Name the blood parasite species.
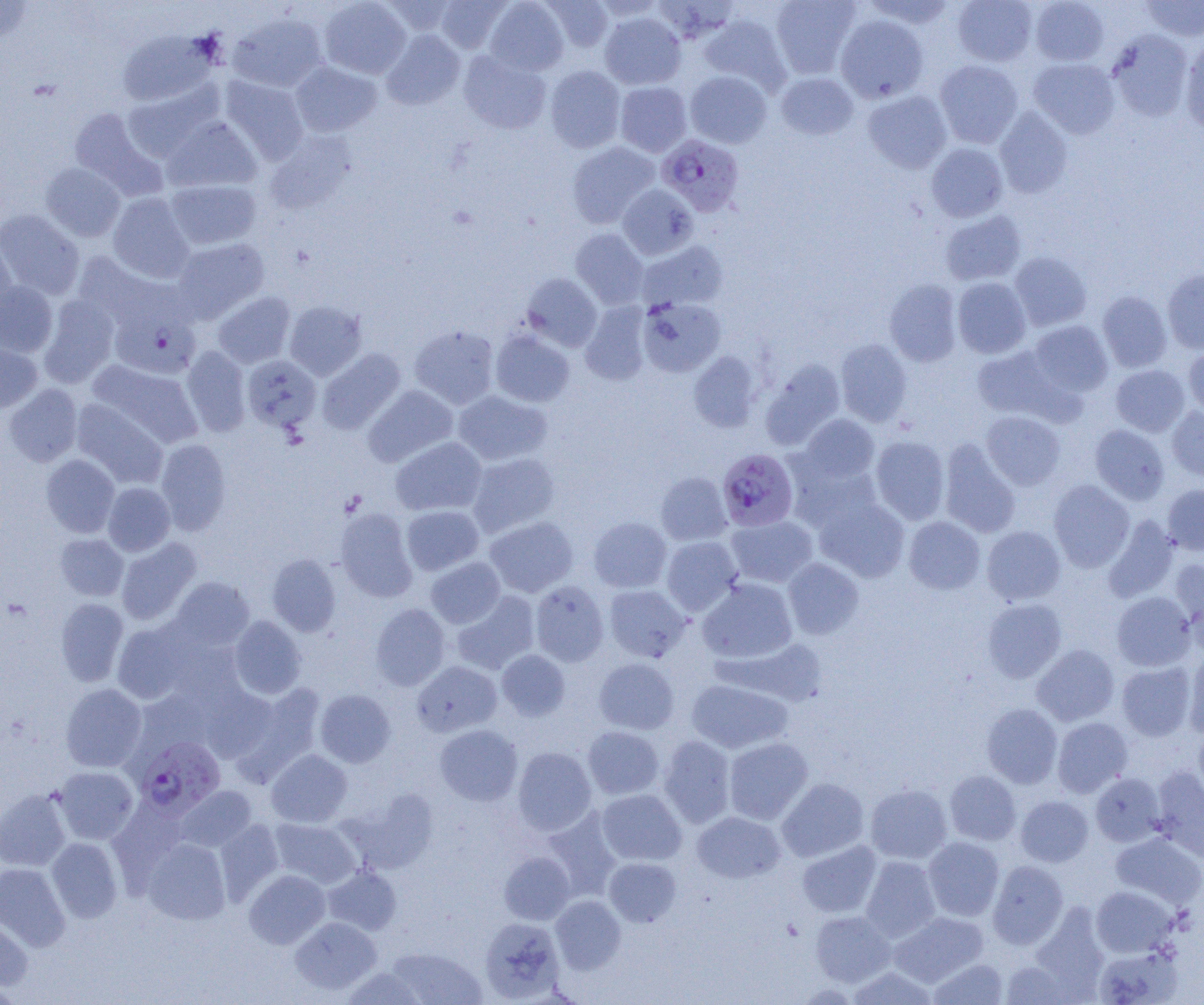

Plasmodium falciparum.

modality = light microscopy
Plasmodium falciparum-infected red blood cell locations = approximate bounding boxes as (x1,y1)-(x2,y2) corner pairs in pixels: (656,134)-(744,216), (110,304)-(201,379), (717,448)-(798,531), (134,737)-(225,817)
image size = 1204×1005 pixels
magnification = 1000x
preparation = thin blood smear
field of view = single
uninfected red blood cell locations = approximate bounding boxes as (x1,y1)-(x2,y2) corner pairs in pixels: (0,0)-(33,45), (319,0)-(411,79), (435,0)-(511,53), (484,0)-(569,76), (541,0)-(613,52), (770,0)-(860,78), (862,0)-(958,29), (952,0)-(1038,66), (1030,0)-(1109,66), (1140,0)-(1204,41), (379,1)-(460,37), (600,12)-(686,90), (229,14)-(327,92), (699,14)-(791,92), (836,14)-(929,103), (117,29)-(216,108), (381,29)-(465,110), (1107,30)-(1194,122), (1179,39)-(1204,133), (459,50)-(551,134), (1028,58)-(1120,139), (935,60)-(1023,148), (290,61)-(382,137), (545,65)-(626,152), (685,71)-(772,148), (775,72)-(859,140), (221,76)-(309,163), (615,81)-(692,156), (123,83)-(222,162), (862,89)-(952,174), (68,107)-(166,200), (993,107)-(1073,198), (162,117)-(262,193), (264,131)-(355,214), (567,141)-(660,228), (926,142)-(1008,222), (41,163)-(125,241), (165,179)-(261,249), (618,184)-(698,260), (108,193)-(194,282), (0,209)-(84,300), (940,210)-(1027,286), (570,228)-(649,309), (0,233)-(17,323), (171,238)-(270,322), (637,240)-(728,312), (72,251)-(175,336), (1009,251)-(1092,331), (1162,269)-(1204,354), (521,273)-(602,351), (952,277)-(1031,358), (884,279)-(962,367), (0,281)-(58,357), (1098,291)-(1171,372), (213,292)-(295,368), (39,295)-(119,388), (637,297)-(726,376), (285,301)-(367,380), (580,302)-(652,385), (1027,321)-(1113,397), (410,324)-(499,409), (491,330)-(575,407), (836,338)-(912,427), (0,339)-(42,414), (972,344)-(1075,423), (1183,344)-(1204,416), (182,346)-(251,436), (317,348)-(406,434), (689,351)-(763,432), (242,355)-(321,433), (760,359)-(846,450), (88,360)-(203,448), (1110,365)-(1190,437), (3,384)-(82,466), (363,385)-(458,467), (453,390)-(552,466), (71,399)-(168,490), (1167,406)-(1204,482), (981,411)-(1066,490), (799,414)-(880,484), (1090,424)-(1169,505), (871,435)-(950,525), (390,437)-(487,516), (155,438)-(231,535), (938,439)-(1021,538), (467,452)-(561,537), (41,454)-(120,537), (785,454)-(883,532), (656,472)-(732,545), (1049,480)-(1134,571), (103,482)-(175,556), (1162,484)-(1204,555), (814,496)-(909,582), (401,505)-(484,575), (334,508)-(418,602), (725,515)-(818,587), (1103,515)-(1180,602), (484,516)-(578,597), (588,516)-(672,593), (904,516)-(985,594), (981,526)-(1065,605), (55,533)-(128,601), (661,536)-(743,615), (116,538)-(201,625), (267,554)-(341,636), (426,557)-(506,628), (783,558)-(864,639), (1170,558)-(1204,638), (169,577)-(254,651), (698,578)-(797,664), (530,580)-(609,666), (604,585)-(691,662), (452,591)-(540,675), (1111,591)-(1196,671), (55,598)-(128,686), (982,599)-(1066,682), (371,603)-(450,690), (228,616)-(306,698), (112,622)-(193,704), (726,638)-(827,705), (1032,644)-(1119,726), (497,649)-(570,721), (1184,649)-(1204,738), (593,658)-(679,734), (412,661)-(502,737), (1117,662)-(1195,741), (686,679)-(792,754), (60,683)-(147,772), (231,683)-(325,780), (202,685)-(280,763), (133,689)-(216,760), (315,689)-(396,767), (981,704)-(1062,788), (1052,717)-(1133,798), (435,724)-(522,806), (583,726)-(664,799), (1194,726)-(1204,806), (658,735)-(736,827), (723,737)-(813,824), (513,747)-(596,835), (266,749)-(352,827), (52,766)-(138,844), (1152,766)-(1204,861), (944,770)-(1020,845), (1090,773)-(1165,846), (777,777)-(869,862), (865,784)-(952,864), (175,785)-(257,852), (0,788)-(72,871), (597,789)-(686,865), (1015,796)-(1093,866), (540,809)-(622,902), (692,811)-(786,884), (270,818)-(361,888), (215,819)-(284,902), (1110,832)-(1204,910), (46,837)-(123,923), (142,837)-(231,925), (923,837)-(1004,920), (797,840)-(881,918), (499,852)-(574,924), (860,856)-(941,942), (604,857)-(681,927), (988,860)-(1068,949), (0,862)-(70,950), (323,865)-(402,935), (244,869)-(330,948), (1091,886)-(1177,957), (550,895)-(626,974), (810,910)-(895,986), (889,911)-(988,986), (0,913)-(33,995), (290,917)-(381,994), (480,917)-(564,1002), (1094,945)-(1183,1005), (386,947)-(486,1004), (999,957)-(1079,1005), (929,958)-(1009,1004), (846,966)-(938,1004), (341,967)-(426,1004)